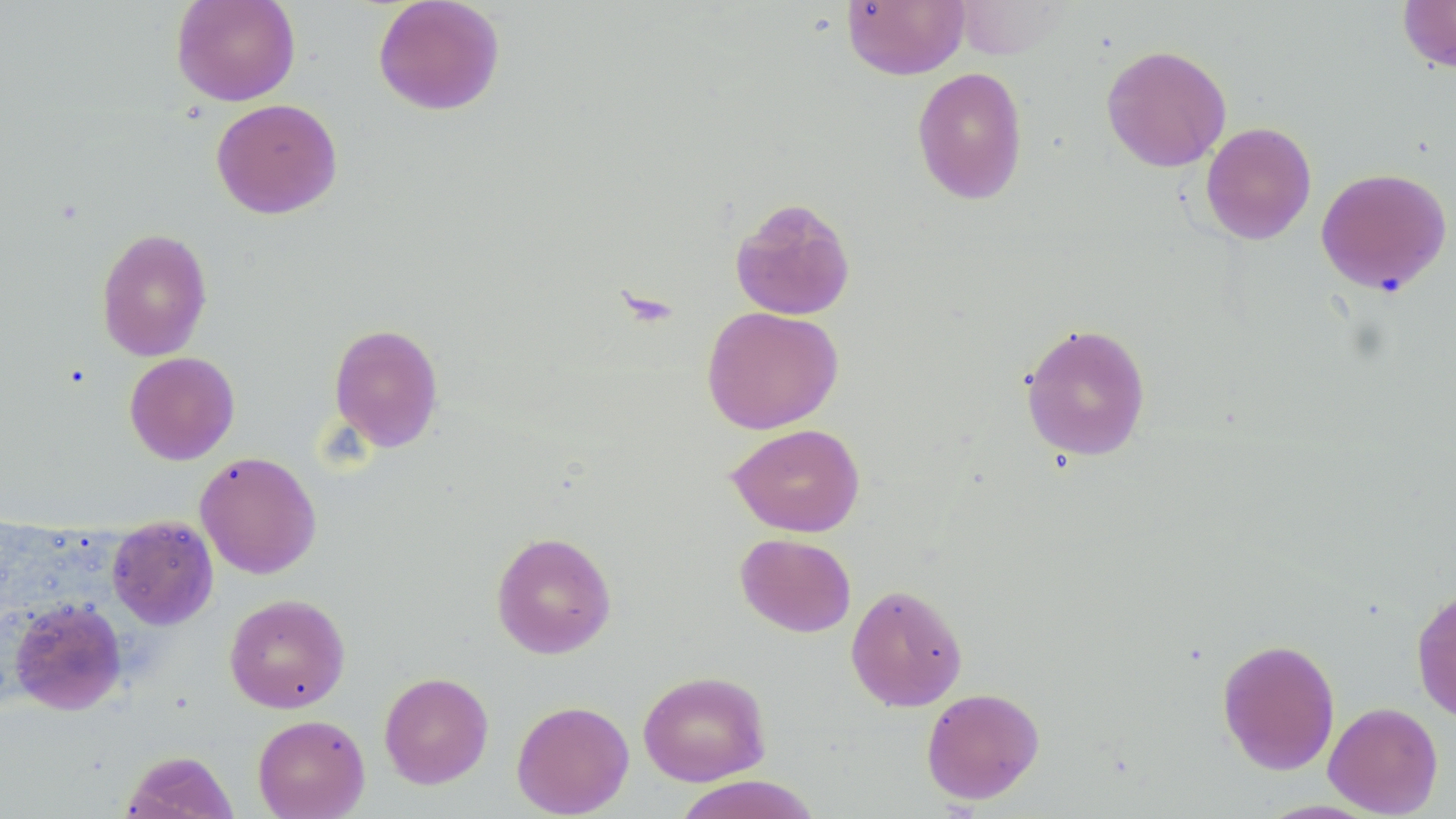

{
  "slide_level_diagnosis": "negative for blood parasites",
  "preparation": "thin blood smear",
  "modality": "light microscopy",
  "field_of_view": "single",
  "magnification": "1000x",
  "uninfected_red_blood_cell_locations": "approximate bounding boxes as named x1/y1/x2/y2 corners in pixels: (x1=171, y1=0, x2=301, y2=106), (x1=372, y1=0, x2=505, y2=116), (x1=841, y1=0, x2=969, y2=80), (x1=1397, y1=0, x2=1456, y2=74), (x1=1101, y1=44, x2=1231, y2=171), (x1=912, y1=66, x2=1028, y2=205), (x1=211, y1=98, x2=343, y2=219), (x1=1200, y1=121, x2=1317, y2=244), (x1=1315, y1=167, x2=1452, y2=295), (x1=730, y1=196, x2=856, y2=321), (x1=96, y1=227, x2=213, y2=361), (x1=701, y1=306, x2=844, y2=434), (x1=1019, y1=322, x2=1151, y2=462), (x1=328, y1=323, x2=444, y2=452), (x1=124, y1=351, x2=240, y2=465), (x1=727, y1=423, x2=865, y2=537), (x1=195, y1=451, x2=322, y2=579), (x1=107, y1=516, x2=218, y2=629), (x1=491, y1=531, x2=617, y2=658), (x1=735, y1=533, x2=856, y2=637), (x1=845, y1=583, x2=968, y2=712), (x1=1410, y1=586, x2=1456, y2=725), (x1=224, y1=593, x2=350, y2=713), (x1=8, y1=598, x2=127, y2=715), (x1=1217, y1=638, x2=1341, y2=775), (x1=638, y1=670, x2=771, y2=786), (x1=379, y1=671, x2=494, y2=789), (x1=920, y1=687, x2=1045, y2=805), (x1=511, y1=700, x2=634, y2=817), (x1=1323, y1=701, x2=1443, y2=817), (x1=252, y1=714, x2=370, y2=819), (x1=121, y1=750, x2=239, y2=819), (x1=672, y1=775, x2=823, y2=819)",
  "stain": "May-Grünwald-Giemsa",
  "image_size": "1456×819 pixels"
}